Locate every Plasmodium falciparum-infected red blood cell.
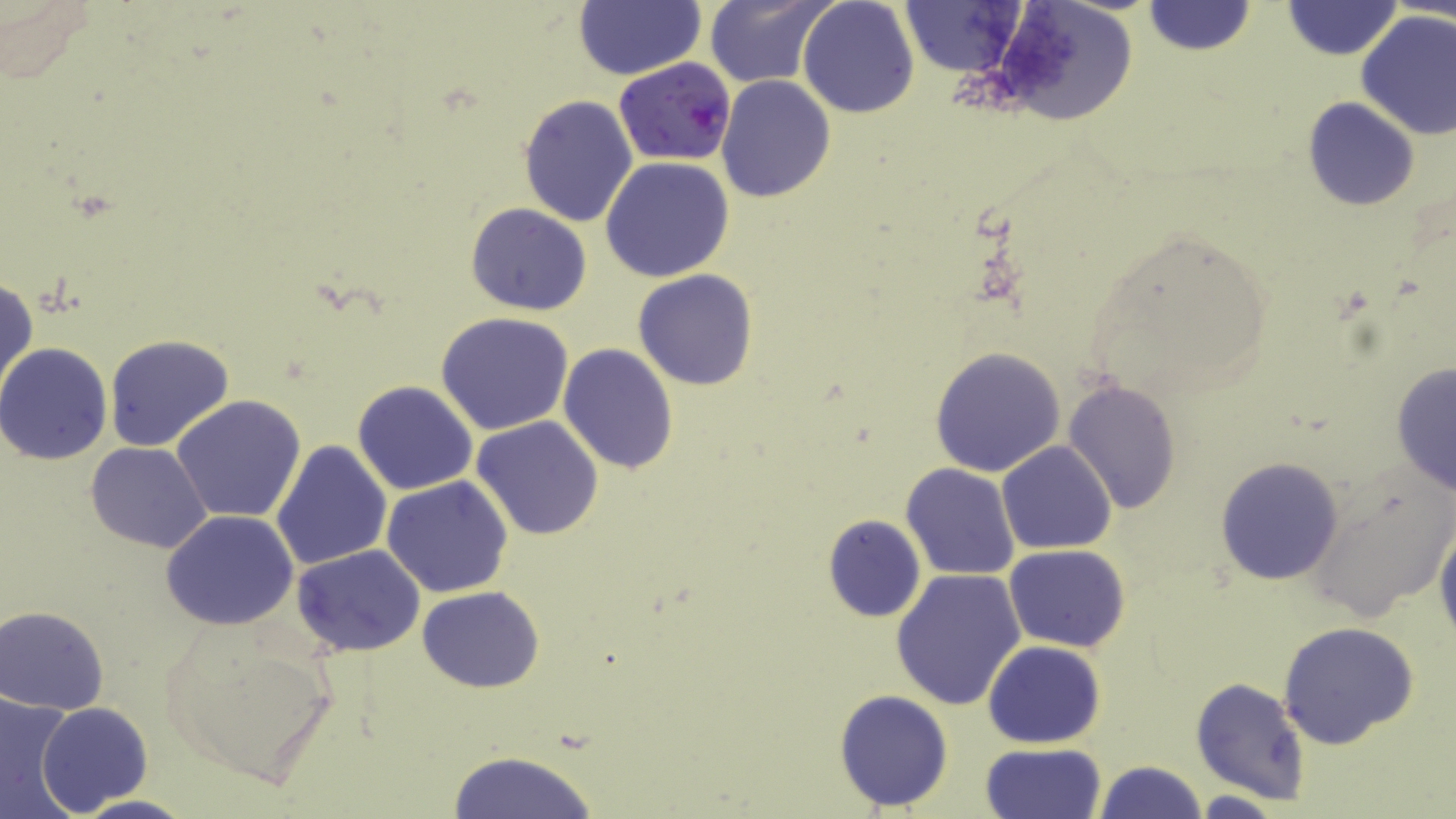
Approximate bounding boxes as (x1, y1, x2, y2) in pixels.
Plasmodium falciparum-infected red blood cells: (615, 57, 738, 166).

slide_level_diagnosis: Plasmodium falciparum
magnification: 1000x
modality: optical microscopy
field_of_view: one of a larger specimen
image_size: 1456×819 pixels
preparation: thin blood film
uninfected_red_blood_cell_locations: 'approximate bounding boxes as (x1, y1, x2, y2) in pixels: (703, 0, 836, 89), (797, 0, 919, 118), (992, 0, 1143, 126), (1281, 0, 1403, 61), (901, 1, 1031, 75), (1143, 1, 1255, 56), (573, 2, 706, 81), (1356, 9, 1456, 140), (715, 76, 835, 203), (517, 95, 638, 228), (1302, 98, 1419, 210), (600, 155, 735, 282), (466, 202, 593, 315), (1075, 224, 1277, 404), (633, 269, 759, 390), (0, 275, 37, 401), (435, 311, 574, 435), (102, 334, 234, 454), (0, 344, 113, 466), (559, 345, 678, 474), (930, 346, 1065, 477), (1389, 362, 1455, 497), (1063, 379, 1182, 516), (354, 380, 477, 495), (172, 394, 307, 524), (471, 415, 603, 540), (272, 438, 394, 572), (996, 440, 1116, 556), (85, 441, 213, 553), (1214, 456, 1346, 586), (901, 464, 1020, 581), (1306, 471, 1454, 622), (382, 476, 514, 597), (160, 510, 300, 628), (822, 515, 926, 622), (1434, 518, 1456, 652), (291, 544, 426, 656), (1004, 544, 1130, 652), (891, 568, 1026, 710), (416, 585, 544, 693), (1, 606, 112, 712), (1277, 622, 1422, 753), (158, 625, 338, 792), (983, 640, 1106, 748), (1190, 677, 1311, 804), (833, 688, 954, 811), (0, 691, 80, 819), (37, 702, 153, 813), (982, 742, 1107, 819), (444, 749, 600, 819), (1093, 760, 1207, 818)'
stain: May-Grünwald-Giemsa